Report the malaria status of this cell.
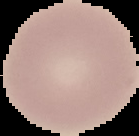

Uninfected.

image_type: segmented cell region on a black background
preparation: thin blood smear
image_size: 139×136 pixels